Classify this cell by malaria status.
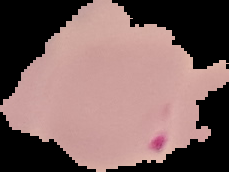
It is parasitized.

{
  "image_size": "229×172 pixels",
  "preparation": "thin blood film",
  "image_type": "cell region segmented out of the field of view; surrounding area masked to black"
}